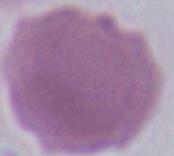 Micrograph. A red blood cell is shown. Captured at 1000x magnification.